Locate every P. falciparum parasite and identify its life-cycle stage.
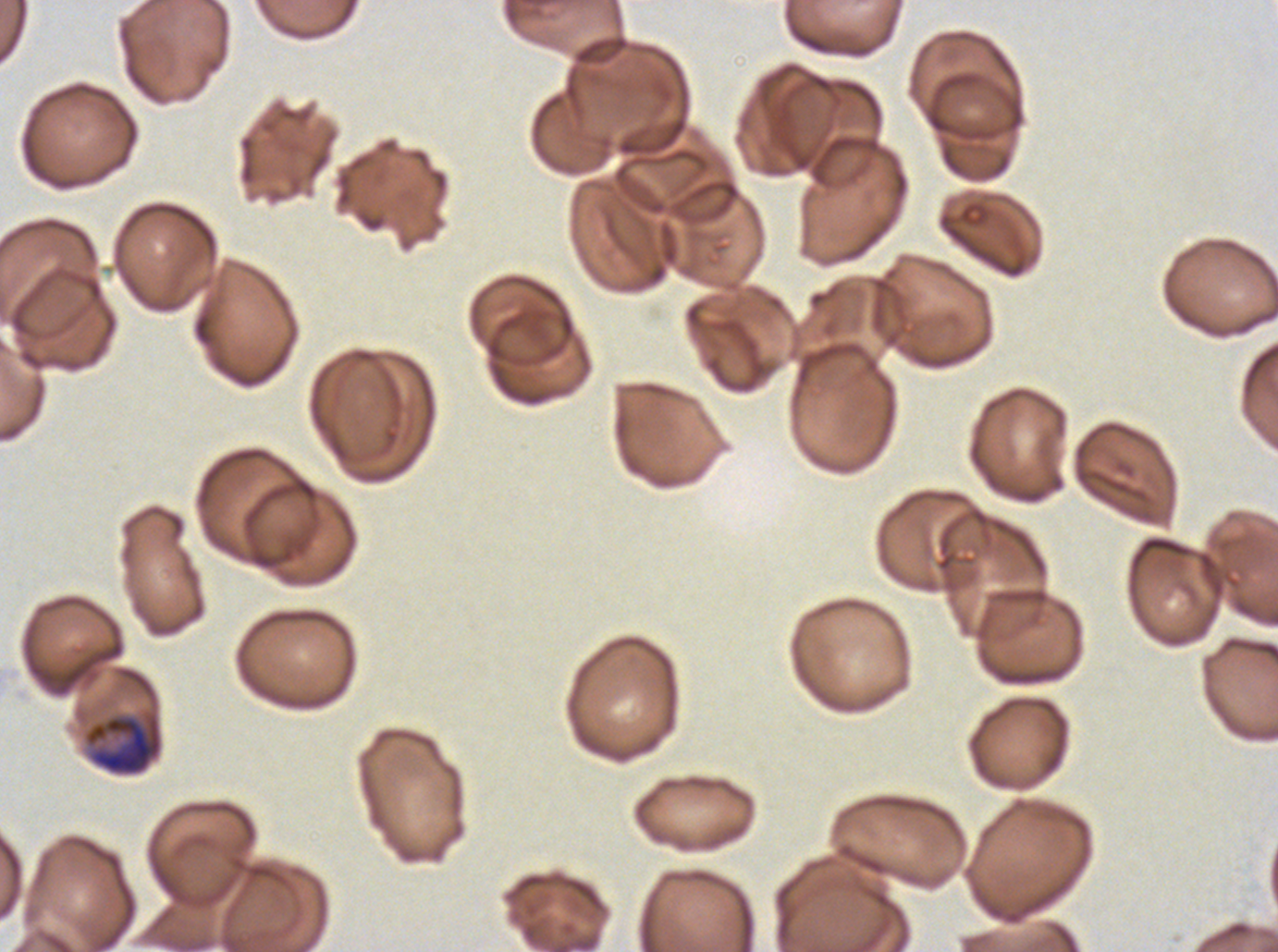
Approximate bounding boxes as [x1, y1, x2, y2] in pixels.
Early schizonts: [82, 710, 164, 776].
No rings, late-ring/early-trophozoite forms, mid trophozoites, late trophozoites, late schizonts, segmenters, or gametocytes observed.

preparation = thin blood smear
field of view = sub-image separated from a larger composite
specimen = P. falciparum from a patient in The Gambia, cultured ex vivo for 24 to 48 hours
image size = 1278×952 pixels
stain = Giemsa